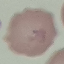
Summary:
  - Malaria status: uninfected
  - Preparation: thin blood smear
  - Stain: Giemsa
  - Image type: cell patch, automatically extracted from a larger field of view and resized to 64 × 64 pixels
  - Capture: smartphone camera at the microscope eyepiece